Classify this cell by malaria status.
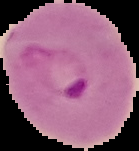
It is parasitized.

{
  "image_size": "139×151 pixels",
  "image_type": "segmented cell region with the area outside set to black",
  "preparation": "thin blood smear"
}